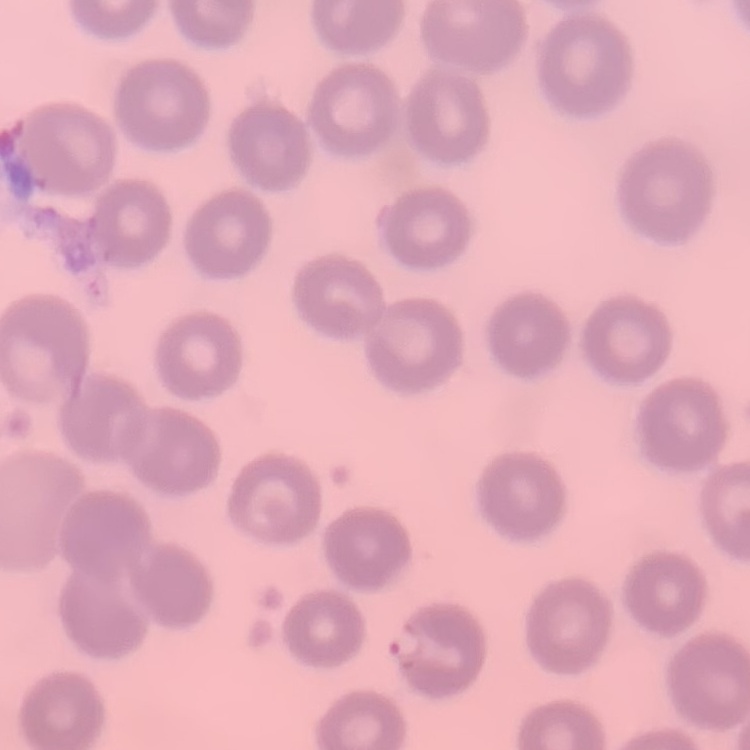
The erythrocytes show no rouleaux formation. Thin peripheral smear. One tile cut from a larger photomicrograph. Field's or Giemsa stain.